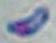

{
  "magnification": "1000x",
  "modality": "micrograph",
  "identification": "Toxoplasma gondii"
}